Mark where platelets are.
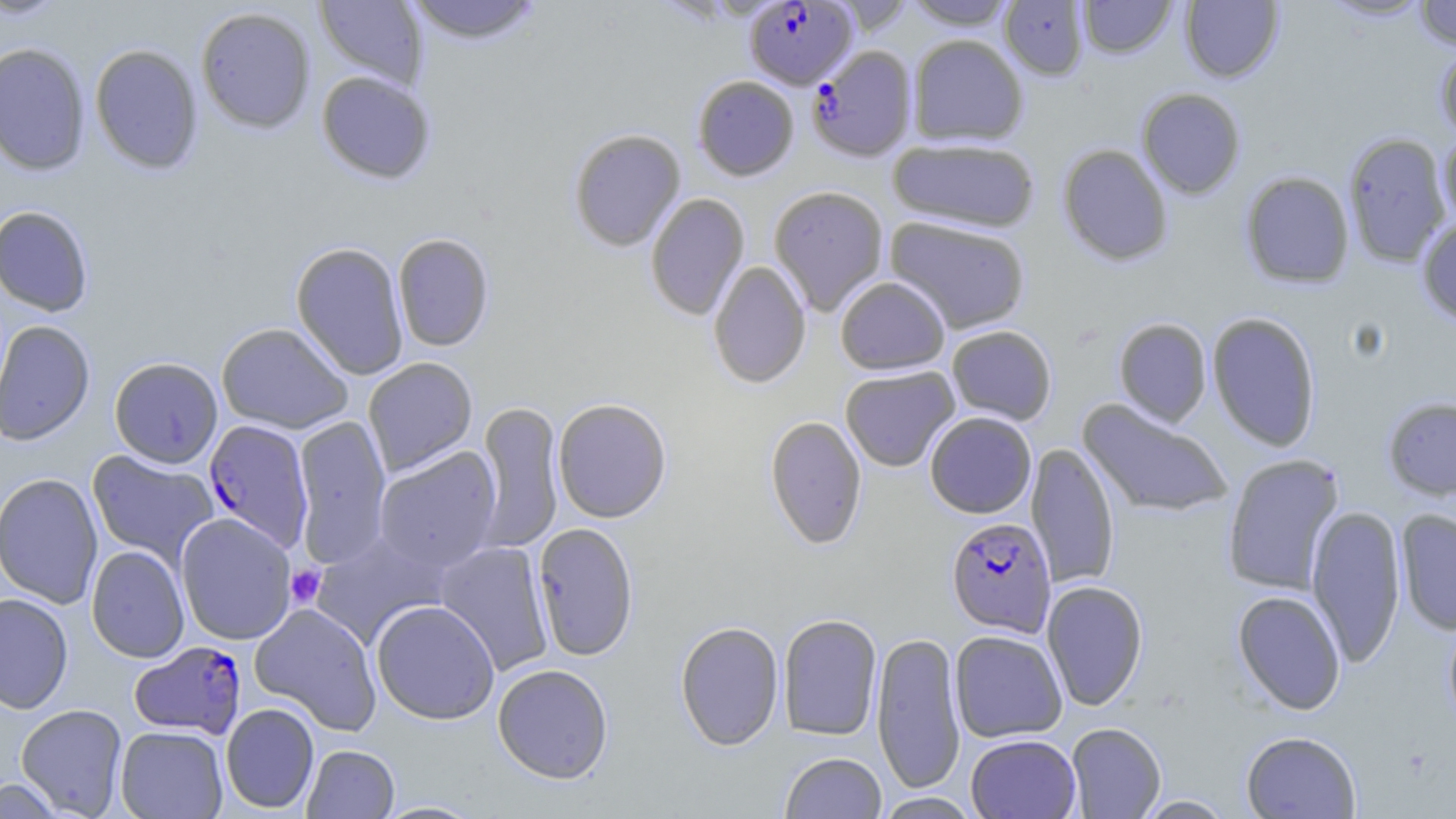

Approximate bounding boxes as [x1, y1, x2, y2] in pixels.
Platelets: [285, 564, 327, 609].

Summary:
  - Uninfected red blood cell locations: [0, 0, 71, 21], [314, 0, 428, 90], [403, 0, 546, 45], [901, 0, 1019, 29], [1077, 0, 1176, 59], [1180, 0, 1284, 83], [1318, 0, 1433, 22], [1414, 0, 1456, 50], [999, 1, 1089, 80], [196, 6, 316, 134], [907, 34, 1028, 147], [0, 42, 91, 176], [90, 44, 203, 175], [1435, 44, 1456, 143], [316, 71, 435, 185], [692, 75, 799, 181], [1136, 88, 1246, 200], [568, 128, 686, 252], [1343, 131, 1452, 267], [1438, 131, 1456, 229], [887, 137, 1041, 233], [1057, 143, 1173, 267], [1240, 171, 1354, 289], [769, 185, 889, 316], [645, 193, 750, 321], [0, 205, 94, 317], [885, 215, 1031, 334], [1417, 217, 1456, 325], [392, 233, 494, 352], [290, 242, 410, 380], [708, 261, 811, 389], [835, 276, 951, 375], [1206, 311, 1322, 451], [1113, 317, 1212, 427], [0, 320, 95, 446], [216, 322, 353, 433], [946, 325, 1057, 425], [109, 357, 223, 468], [363, 357, 478, 476], [840, 366, 960, 472], [552, 397, 672, 523], [1382, 397, 1456, 500], [1077, 400, 1234, 519], [474, 402, 564, 553], [925, 412, 1037, 518], [292, 415, 391, 567], [764, 415, 867, 550], [1026, 442, 1120, 589], [373, 447, 502, 573], [87, 450, 218, 568], [1222, 453, 1345, 596], [0, 473, 104, 609], [1307, 504, 1406, 668], [1395, 508, 1456, 636], [175, 513, 297, 645], [532, 522, 639, 662], [309, 529, 450, 649], [435, 540, 554, 676], [86, 545, 189, 663], [1041, 580, 1148, 711], [1232, 590, 1346, 714], [0, 593, 74, 714], [371, 599, 500, 724], [249, 602, 383, 735], [777, 613, 883, 741], [1443, 615, 1456, 732], [675, 621, 784, 751], [950, 629, 1067, 743], [872, 631, 966, 794], [492, 664, 614, 784], [16, 703, 128, 817], [221, 703, 319, 813], [1065, 722, 1165, 818], [115, 725, 228, 819], [1241, 731, 1361, 818], [966, 733, 1081, 819], [302, 744, 399, 818], [780, 752, 887, 818], [0, 777, 68, 818], [873, 792, 982, 818], [1133, 795, 1237, 818], [373, 800, 487, 819]
  - Plasmodium falciparum-infected red blood cell locations: [744, 1, 858, 89], [807, 46, 917, 162], [204, 419, 314, 552], [946, 516, 1057, 636], [129, 640, 247, 739]
  - Slide-level diagnosis: Plasmodium falciparum
  - Modality: light microscopy
  - Image size: 1456×819 pixels
  - Field of view: one of a larger specimen
  - Stain: May-Grünwald-Giemsa
  - Preparation: thin blood film
  - Magnification: 1000x